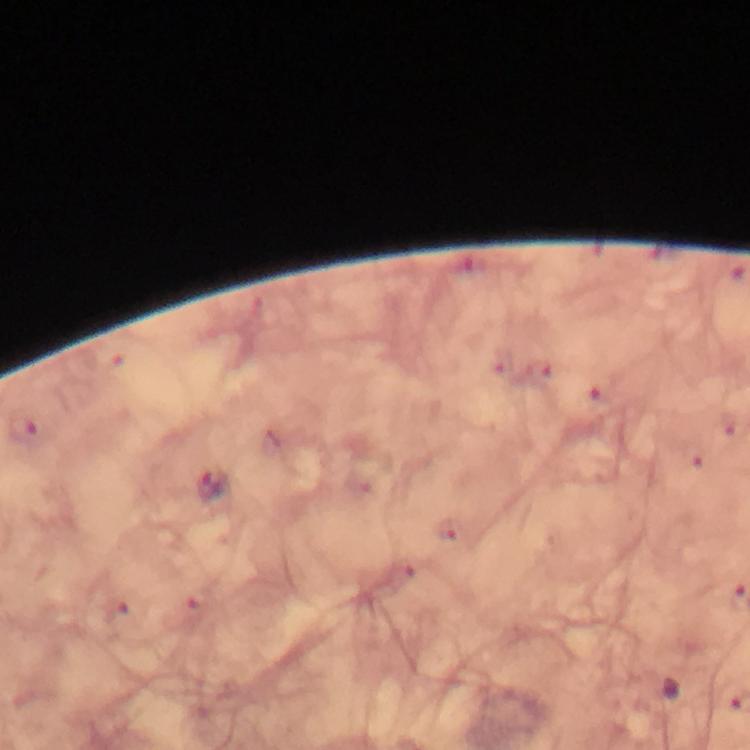
Approximate object centers, in pixels from the top-left corner.
Summary:
  - Plasmodium parasite locations: (x=28, y=429), (x=210, y=487)
  - Context: from a malaria diagnostic workup
  - Stain: Giemsa
  - Preparation: thick blood film
  - Cropped from: a single field of view
  - Magnification: 100x
  - Immersion oil: used
  - Image size: 750×750 pixels
  - Capture: smartphone mounted on the microscope